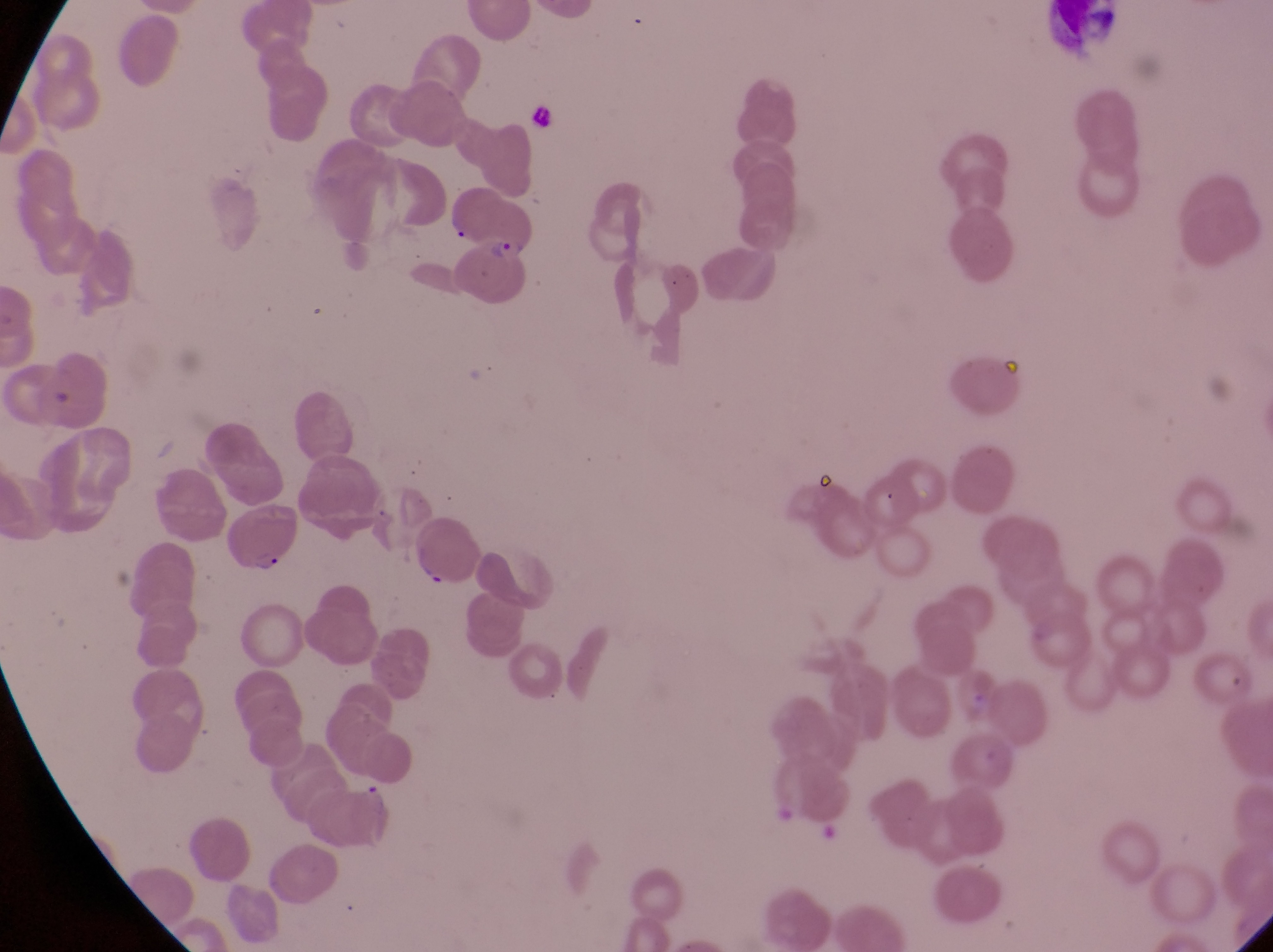

image size = 1273×952 pixels
field of view = single
object labeled both artifact (platelet-like body, stain precipitate, or debris) and parasitised red blood cell by the source = approximate bounding boxes as [left, top, right, bottom] in pixels: [417, 557, 452, 594]
preparation = thin blood smear
capture = smartphone photograph through the eyepiece of an Olympus CX-23 microscope
country = Uganda
parasitised red blood cell locations = approximate bounding boxes as [left, top, right, bottom] in pixels: [462, 235, 539, 309], [224, 507, 304, 577]
magnification = 1000x